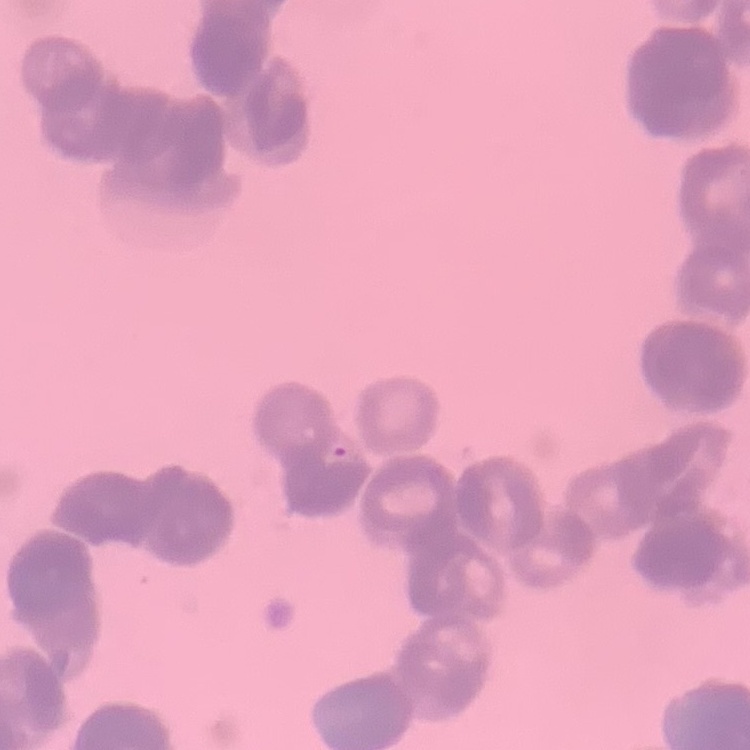

erythrocyte_morphology: rouleaux formation
stain: Field's or Giemsa
image_type: one tile cut from a larger photomicrograph
preparation: thin peripheral smear